Assess this cell for malaria.
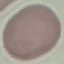

It is uninfected.

Summary:
  - Image type: cell patch, automatically extracted from a larger field of view and resized to 64 × 64 pixels
  - Preparation: thin blood film
  - Capture: smartphone through the microscope eyepiece
  - Stain: Giemsa